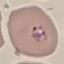

Malaria status: parasitized. Giemsa stain. Acquired by smartphone through the microscope eyepiece. Automatically extracted cell patch, resized to 64 × 64 pixels. Thin blood smear.